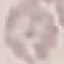 Malaria status: uninfected. Acquired by smartphone through the microscope eyepiece. Thin blood smear. Automatically extracted cell patch, resized to 64 × 64 pixels. Giemsa-stained preparation.